Assess this cell for malaria.
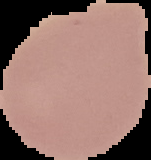
It is uninfected.

Summary:
  - Preparation: thin blood smear
  - Image type: segmented cell region with the area outside set to black
  - Image size: 151×160 pixels